Report the malaria status of this cell.
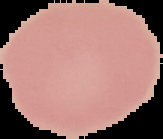
Uninfected.

{
  "preparation": "thin blood film",
  "image_size": "163×139 pixels",
  "image_type": "segmented cell region with the area outside set to black"
}